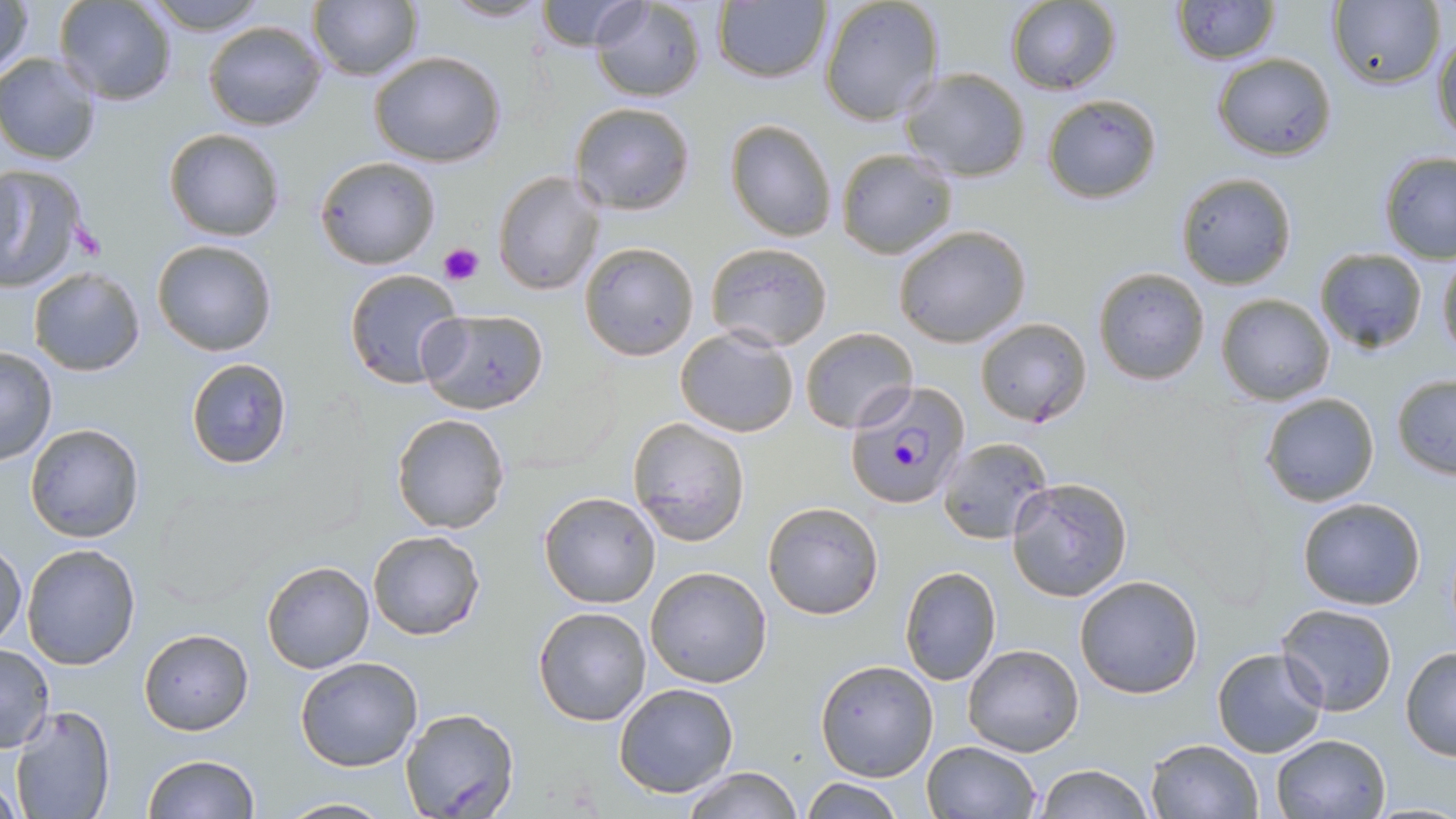

Summary:
  - Coordinate format: approximate bounding boxes as [x1, y1, x2, y2] in pixels
  - Uninfected red blood cell locations: [0, 0, 34, 84], [141, 0, 271, 34], [308, 0, 423, 83], [532, 0, 647, 51], [588, 0, 708, 103], [817, 0, 946, 126], [1004, 0, 1121, 94], [55, 1, 178, 106], [440, 1, 552, 23], [1171, 1, 1280, 65], [1332, 1, 1446, 90], [712, 2, 831, 84], [202, 19, 328, 132], [1432, 28, 1456, 146], [1, 51, 102, 165], [369, 51, 508, 167], [1212, 53, 1336, 161], [900, 66, 1032, 182], [1041, 94, 1161, 203], [570, 101, 696, 216], [514, 107, 659, 264], [724, 118, 837, 242], [163, 128, 287, 242], [835, 147, 958, 259], [1378, 151, 1456, 263], [315, 155, 441, 269], [0, 165, 88, 293], [493, 170, 605, 296], [1175, 172, 1298, 288], [894, 226, 1031, 349], [151, 238, 279, 357], [704, 241, 833, 350], [579, 242, 700, 360], [1314, 246, 1428, 354], [1437, 253, 1456, 363], [1092, 266, 1212, 386], [343, 267, 465, 389], [28, 268, 145, 376], [1216, 293, 1334, 405], [418, 308, 550, 413], [975, 317, 1092, 428], [673, 325, 802, 439], [799, 328, 919, 434], [0, 346, 57, 466], [186, 357, 292, 469], [1390, 373, 1455, 480], [1260, 392, 1380, 508], [391, 412, 510, 534], [627, 418, 752, 546], [24, 422, 144, 543], [938, 437, 1053, 543], [1008, 477, 1133, 601], [538, 491, 663, 609], [1296, 497, 1426, 609], [762, 500, 885, 621], [368, 531, 484, 641], [0, 543, 25, 651], [21, 543, 142, 668], [262, 561, 373, 673], [899, 565, 1003, 686], [645, 566, 772, 688], [1073, 574, 1204, 698], [1278, 603, 1397, 715], [533, 606, 653, 728], [138, 627, 253, 734], [0, 642, 54, 752], [962, 644, 1084, 756], [1400, 646, 1456, 760], [1211, 647, 1328, 758], [294, 656, 424, 772], [815, 659, 938, 782], [613, 682, 739, 797], [8, 705, 118, 819], [399, 708, 521, 819], [1270, 733, 1390, 818], [1144, 737, 1264, 819], [921, 740, 1042, 818], [142, 754, 260, 819], [677, 765, 800, 819], [1034, 765, 1153, 819], [798, 777, 904, 818], [276, 797, 396, 817]
  - Plasmodium falciparum-infected red blood cell locations: [847, 380, 972, 510]
  - Platelet locations: [69, 224, 105, 260], [438, 242, 483, 286]
  - Slide-level diagnosis: Plasmodium falciparum
  - Image size: 1456×819 pixels
  - Stain: May-Grünwald-Giemsa
  - Field of view: one of a larger specimen
  - Preparation: thin blood smear
  - Modality: light microscopy
  - Magnification: 1000x